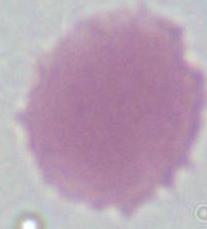

Summary:
  - Modality: photomicrograph
  - Identification: erythrocyte
  - Magnification: 1000x